Assess the morphology of the red blood cells.
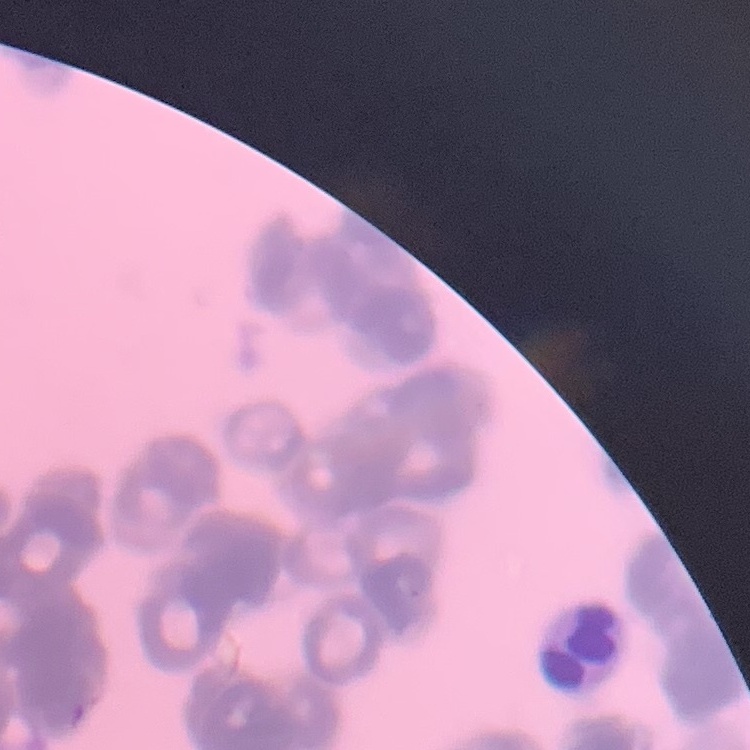
Rouleaux formation.

One tile cut from a larger photomicrograph. Field's or Giemsa stain. Thin peripheral smear.